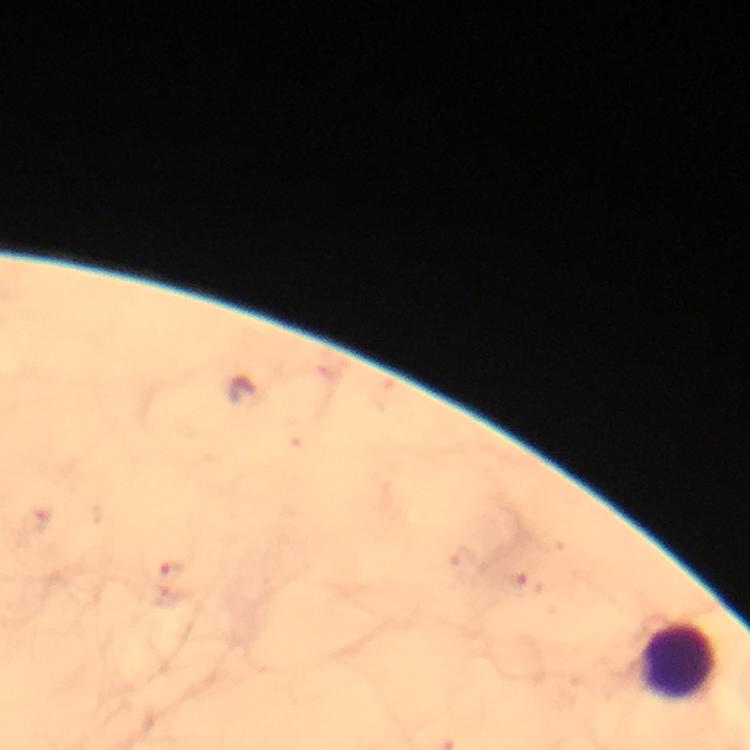
Approximate centers as (x, y) in pixels.
Summary:
  - Leukocyte locations: (681, 660)
  - Malaria parasite locations: (171, 569)
  - Preparation: thick blood film
  - Immersion oil: used
  - Capture: smartphone camera through the microscope
  - Cropped from: a single field of view
  - Context: from a diagnostic examination for malaria
  - Stain: Giemsa
  - Image size: 750×750 pixels
  - Magnification: 100x